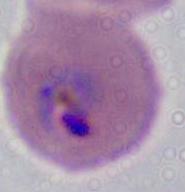
Summary:
  - Modality: micrograph
  - Magnification: 400x or 1000x
  - Identification: Plasmodium